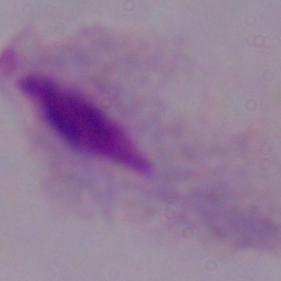
{
  "modality": "photomicrograph",
  "magnification": "1000x",
  "identification": "trichomonad"
}